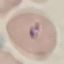

malaria_status: parasitized
preparation: thin smear
image_type: automatically extracted cell patch, resized to 64 × 64 pixels
capture: smartphone through the microscope eyepiece
stain: Giemsa